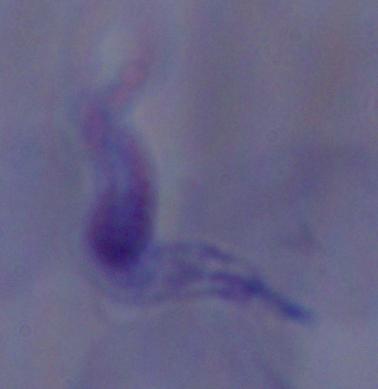 A trypanosome is seen. Photomicrograph. 1000x magnification.